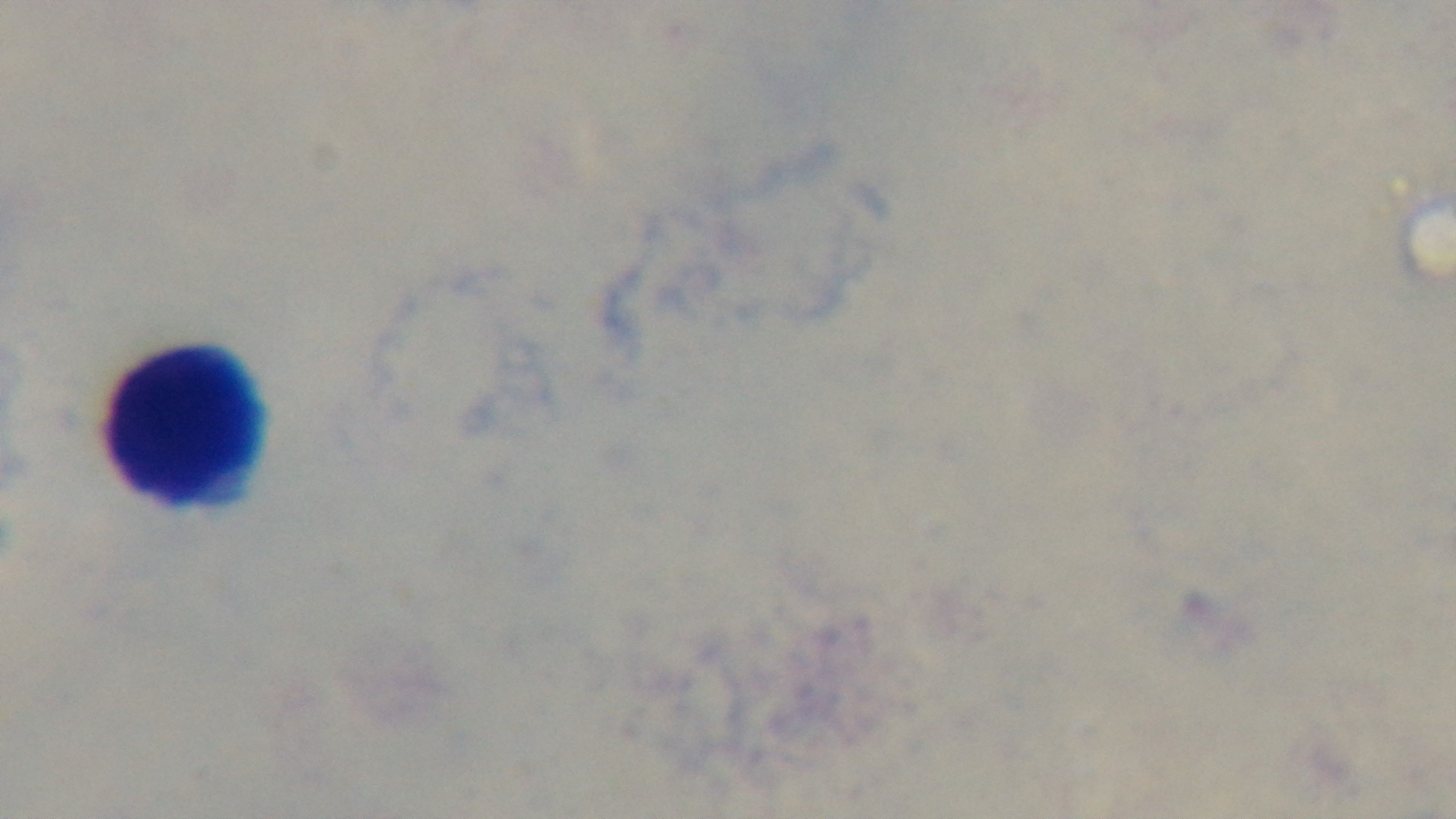

Summary:
  - Stain: Giemsa
  - Objective: 100x oil immersion
  - Modality: light microscopy
  - Malaria status: negative
  - Preparation: thick blood film
  - Field of view: single
  - Capture: mounted 4K digital camera